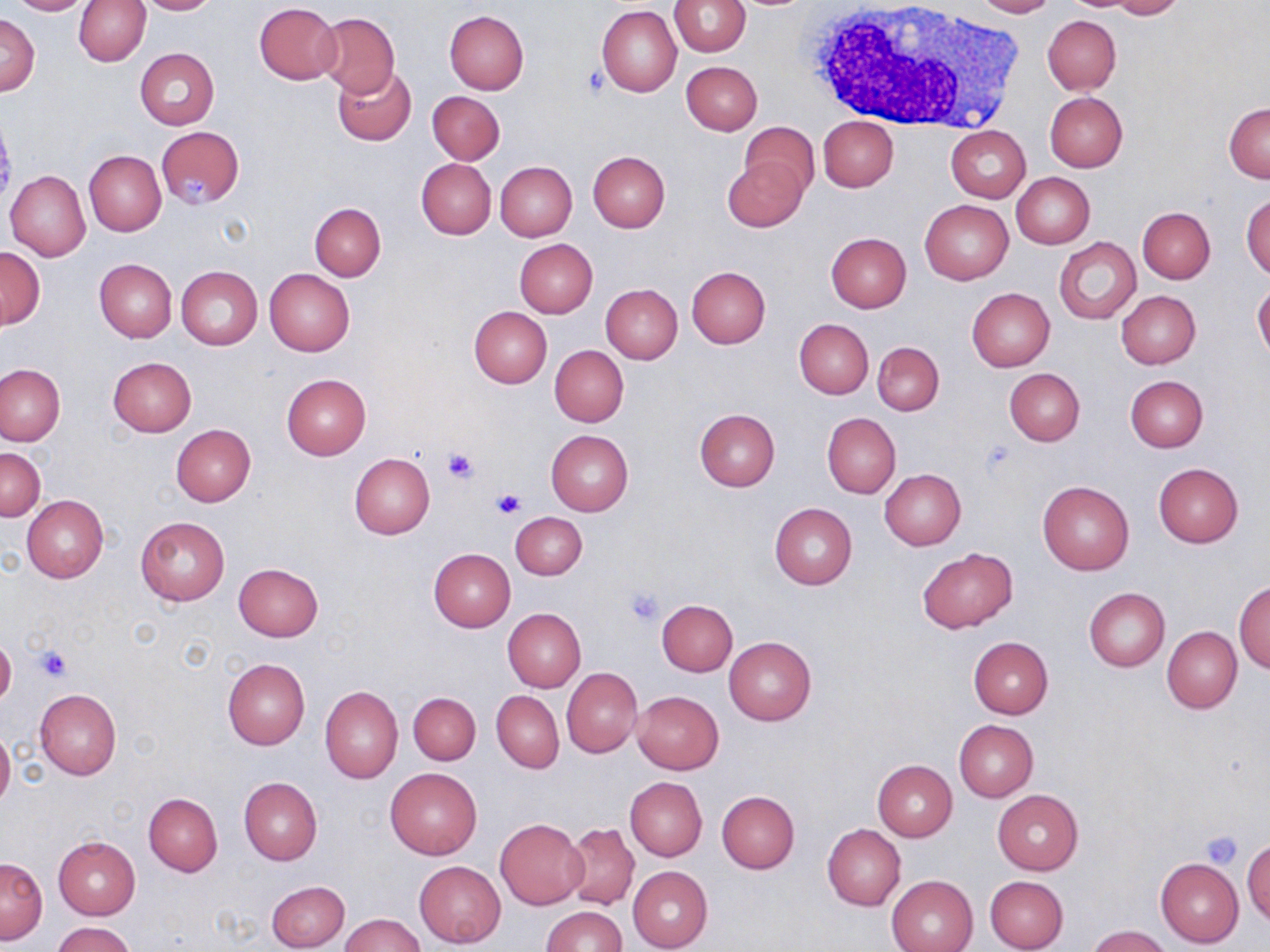
Approximate bounding boxes as (x1, y1, x2, y2) in pixels. Platelet locations: (582, 64, 609, 98), (179, 174, 209, 202), (441, 447, 481, 484), (491, 487, 524, 520), (623, 587, 665, 626), (37, 646, 71, 681), (1199, 831, 1243, 869). Uninfected red blood cell locations: (7, 0, 94, 15), (74, 0, 150, 66), (134, 0, 220, 14), (670, 0, 750, 56), (968, 0, 1057, 17), (1108, 0, 1184, 19), (254, 3, 342, 84), (597, 5, 681, 97), (443, 10, 530, 95), (315, 12, 400, 97), (2, 15, 39, 95), (1043, 15, 1121, 93), (136, 49, 219, 129), (680, 61, 762, 135), (333, 65, 417, 146), (427, 91, 505, 163), (1044, 91, 1127, 172), (1225, 102, 1270, 182), (818, 116, 898, 192), (740, 121, 819, 200), (156, 125, 245, 209), (947, 125, 1030, 202), (83, 150, 165, 237), (588, 151, 670, 234), (722, 156, 807, 233), (416, 157, 496, 239), (495, 162, 577, 241), (6, 171, 90, 261), (1011, 172, 1094, 249), (1242, 191, 1270, 280), (919, 200, 1013, 285), (309, 204, 385, 281), (1137, 207, 1215, 283), (826, 232, 912, 313), (1055, 237, 1142, 325), (514, 239, 598, 318), (0, 248, 44, 328), (95, 259, 176, 342), (176, 266, 262, 350), (687, 267, 770, 349), (264, 268, 355, 356), (600, 283, 682, 363), (1253, 283, 1270, 362), (967, 288, 1054, 371), (1116, 290, 1201, 369), (469, 307, 551, 387), (794, 318, 874, 399), (873, 342, 944, 415), (549, 345, 629, 426), (108, 357, 197, 437), (0, 363, 64, 445), (1004, 368, 1084, 446), (282, 374, 371, 459), (1125, 375, 1208, 452), (694, 408, 780, 491), (822, 412, 901, 498), (171, 424, 254, 506), (546, 430, 634, 515), (0, 447, 45, 521), (349, 453, 435, 539), (1153, 462, 1244, 547), (880, 469, 965, 551), (1037, 481, 1134, 574), (22, 496, 108, 582), (769, 503, 857, 590), (511, 512, 587, 580), (136, 516, 230, 605), (917, 547, 1017, 633), (429, 549, 515, 631), (233, 563, 324, 640), (1234, 580, 1270, 672), (1084, 588, 1170, 672), (657, 600, 738, 676), (503, 608, 586, 692), (1163, 627, 1242, 713), (0, 637, 16, 706), (723, 637, 816, 726), (969, 637, 1053, 718), (222, 658, 309, 750), (562, 669, 642, 757), (320, 685, 403, 782), (34, 688, 122, 779), (492, 691, 563, 773), (631, 691, 724, 775), (408, 692, 480, 763), (954, 720, 1038, 801), (0, 728, 14, 809), (873, 759, 957, 840), (385, 767, 482, 859), (239, 777, 322, 865), (624, 777, 707, 861), (992, 789, 1083, 875), (716, 790, 800, 874), (143, 793, 223, 876), (495, 818, 587, 910), (563, 822, 640, 910), (822, 824, 906, 910), (54, 837, 140, 919), (1243, 839, 1270, 927), (0, 857, 48, 944), (1156, 858, 1244, 948), (415, 860, 505, 947), (628, 866, 713, 951), (887, 875, 978, 952), (984, 875, 1069, 952), (265, 880, 349, 951), (541, 905, 627, 952), (342, 914, 423, 951), (52, 921, 136, 952), (1087, 925, 1172, 952). White blood cell locations: (807, 0, 1022, 133). Slide-level diagnosis: negative for blood parasites. Light microscopy. Thin blood smear. Image is 1270×952 pixels. May-Grünwald-Giemsa-stained preparation. One field of a larger specimen. Captured at 1000x magnification.